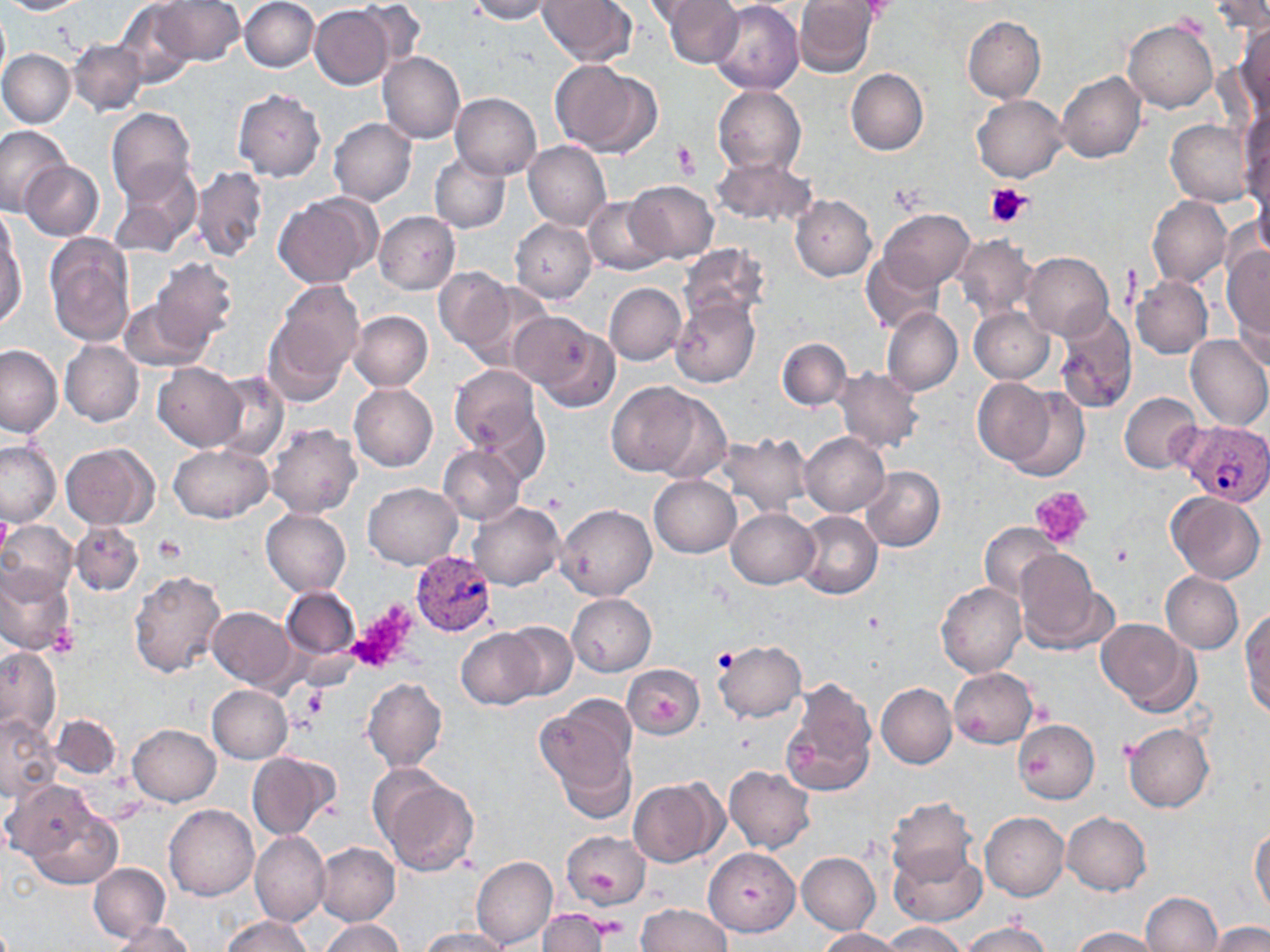

Summary:
  - Coordinate format: approximate bounding boxes as (x1, y1, x2, y2) in pixels
  - Platelet locations: (672, 140, 699, 180), (986, 182, 1034, 227), (887, 184, 931, 216), (1030, 486, 1094, 548), (0, 511, 11, 555), (153, 535, 187, 565), (1111, 544, 1133, 569), (347, 609, 415, 672), (47, 625, 80, 657), (713, 649, 738, 672), (300, 686, 329, 718)
  - Plasmodium vivax-infected red blood cell locations: (1180, 421, 1270, 505), (411, 551, 498, 636)
  - Uninfected red blood cell locations: (0, 0, 87, 15), (239, 0, 320, 72), (354, 0, 429, 71), (468, 0, 553, 23), (538, 0, 636, 65), (661, 0, 741, 68), (793, 0, 877, 76), (1210, 0, 1270, 34), (151, 1, 245, 66), (643, 1, 726, 25), (709, 1, 804, 94), (115, 4, 197, 86), (311, 4, 393, 88), (0, 5, 10, 88), (963, 16, 1046, 103), (1123, 20, 1218, 113), (1234, 24, 1270, 120), (68, 38, 148, 117), (0, 49, 75, 128), (378, 52, 465, 145), (549, 59, 660, 156), (846, 68, 928, 155), (1056, 72, 1145, 163), (711, 85, 805, 175), (232, 88, 326, 181), (450, 92, 542, 180), (972, 94, 1069, 183), (104, 107, 197, 203), (1239, 108, 1269, 209), (328, 118, 418, 206), (1166, 118, 1257, 207), (0, 124, 71, 214), (307, 124, 404, 254), (523, 141, 611, 231), (430, 152, 510, 234), (709, 155, 817, 228), (20, 162, 104, 240), (109, 162, 202, 256), (191, 166, 270, 263), (1254, 174, 1270, 262), (628, 181, 718, 262), (273, 193, 378, 288), (583, 195, 669, 275), (790, 195, 876, 281), (1148, 196, 1232, 287), (0, 207, 20, 292), (374, 210, 460, 294), (880, 210, 974, 288), (510, 219, 595, 303), (1, 230, 27, 331), (43, 232, 137, 347), (952, 235, 1037, 319), (678, 244, 768, 326), (1221, 247, 1270, 342), (861, 251, 944, 335), (1022, 252, 1112, 340), (152, 257, 239, 348), (434, 267, 515, 353), (1131, 274, 1212, 359), (463, 277, 555, 370), (604, 282, 686, 365), (265, 284, 362, 399), (1232, 292, 1270, 373), (118, 297, 209, 372), (671, 298, 759, 388), (969, 306, 1054, 384), (882, 307, 962, 395), (1054, 308, 1137, 414), (348, 311, 433, 391), (512, 311, 618, 408), (1184, 335, 1270, 432), (777, 337, 852, 411), (59, 340, 144, 427), (0, 345, 63, 437), (153, 363, 246, 450), (448, 364, 545, 461), (832, 366, 925, 453), (208, 371, 289, 461), (974, 379, 1054, 467), (350, 382, 437, 472), (607, 382, 703, 478), (1003, 387, 1090, 483), (650, 389, 733, 483), (1120, 392, 1202, 474), (265, 423, 361, 519), (800, 431, 890, 516), (717, 433, 813, 515), (0, 440, 61, 526), (60, 443, 157, 529), (167, 444, 273, 522), (438, 445, 524, 524), (861, 467, 945, 550), (648, 474, 741, 558), (363, 483, 461, 569), (1167, 491, 1266, 583), (468, 501, 564, 590), (557, 503, 656, 600), (726, 507, 818, 589), (260, 508, 351, 597), (796, 510, 881, 599), (0, 519, 79, 598), (71, 520, 143, 591), (978, 523, 1062, 604), (1013, 550, 1105, 652), (0, 563, 75, 654), (129, 569, 227, 677), (1161, 572, 1243, 654), (935, 582, 1026, 678), (282, 586, 360, 659), (567, 594, 656, 675), (208, 607, 294, 688), (1240, 610, 1270, 716), (1096, 618, 1197, 715), (498, 623, 577, 701), (457, 628, 547, 710), (712, 640, 806, 722), (0, 647, 60, 740), (623, 664, 704, 739), (948, 667, 1037, 748), (362, 678, 447, 772), (780, 678, 876, 798), (875, 683, 956, 769), (206, 685, 293, 763), (536, 696, 637, 797), (49, 714, 119, 779), (0, 715, 60, 798), (1013, 720, 1099, 803), (1123, 722, 1215, 812), (128, 723, 221, 806), (555, 745, 637, 824), (248, 751, 339, 841), (724, 766, 815, 854), (374, 770, 478, 876), (627, 778, 723, 866), (16, 793, 122, 890), (885, 797, 976, 885), (164, 804, 258, 901), (980, 812, 1068, 900), (1062, 812, 1151, 895), (1250, 826, 1270, 916), (250, 831, 330, 925), (562, 831, 650, 910), (315, 842, 401, 925), (890, 846, 986, 926), (704, 847, 801, 937), (796, 851, 880, 934), (471, 855, 557, 948), (88, 863, 169, 941), (1140, 892, 1222, 951), (635, 903, 732, 952), (535, 910, 609, 952), (220, 915, 313, 952), (318, 918, 403, 952), (111, 920, 194, 951), (959, 921, 1053, 952), (882, 922, 966, 952), (1207, 922, 1270, 952), (1070, 926, 1162, 952), (419, 928, 510, 952), (819, 928, 904, 951)
  - Slide-level diagnosis: Plasmodium vivax
  - Image size: 1270×952 pixels
  - Stain: May-Grünwald-Giemsa
  - Preparation: thin blood smear
  - Field of view: one of a larger specimen
  - Modality: light microscopy
  - Magnification: 1000x